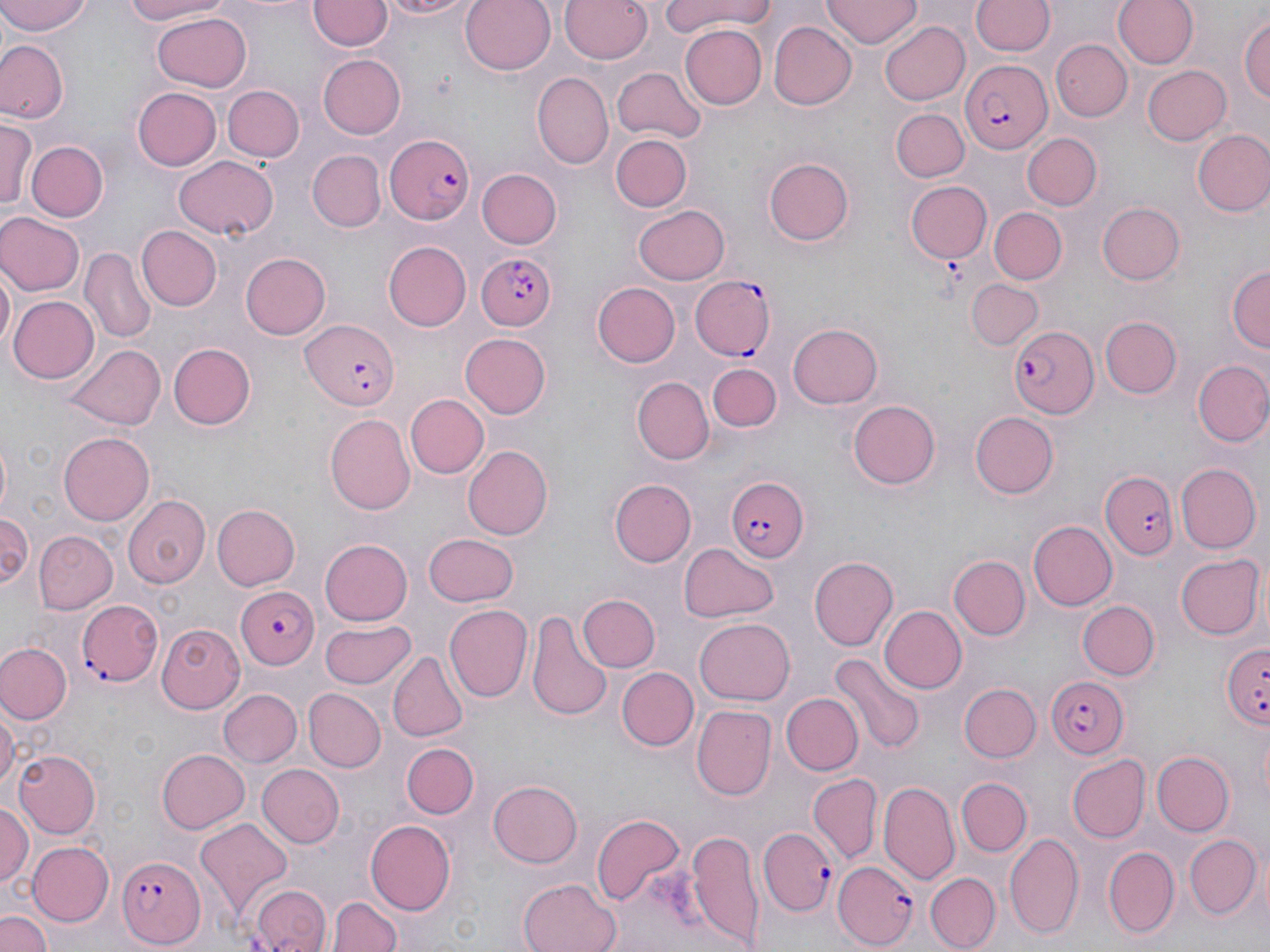

Approximate bounding boxes as (x1, y1, x2, y2) in pixels. Platelet locations: (937, 258, 969, 293). Plasmodium falciparum-infected red blood cell locations: (960, 59, 1052, 155), (382, 131, 473, 226), (473, 250, 558, 331), (690, 274, 776, 360), (301, 320, 399, 410), (1009, 324, 1100, 419), (1103, 472, 1175, 561), (725, 476, 808, 561), (234, 587, 320, 670), (76, 599, 162, 686), (1219, 642, 1268, 732), (1046, 676, 1130, 756), (757, 829, 834, 916), (118, 853, 205, 948), (832, 862, 920, 948). Uninfected red blood cell locations: (0, 0, 94, 36), (116, 0, 229, 25), (375, 0, 474, 18), (459, 0, 556, 75), (558, 0, 655, 63), (660, 0, 773, 37), (821, 0, 923, 49), (1114, 0, 1199, 70), (308, 1, 389, 52), (972, 1, 1054, 58), (152, 10, 251, 90), (1239, 10, 1270, 104), (881, 19, 970, 104), (769, 21, 857, 109), (678, 23, 767, 109), (0, 39, 68, 123), (1050, 39, 1131, 122), (317, 54, 407, 139), (1141, 66, 1232, 145), (613, 67, 706, 142), (535, 72, 615, 167), (221, 84, 304, 163), (133, 88, 221, 170), (891, 108, 968, 183), (0, 120, 34, 214), (1192, 128, 1270, 217), (1021, 133, 1101, 210), (610, 134, 692, 211), (26, 140, 109, 221), (308, 150, 386, 232), (173, 155, 278, 241), (765, 158, 855, 245), (475, 169, 559, 249), (906, 180, 993, 265), (1096, 201, 1184, 285), (634, 203, 731, 284), (989, 207, 1066, 285), (0, 212, 81, 296), (138, 225, 221, 310), (384, 242, 472, 330), (82, 246, 155, 345), (238, 251, 331, 340), (0, 264, 14, 358), (1227, 266, 1268, 355), (967, 279, 1044, 349), (594, 282, 680, 367), (9, 294, 99, 384), (1099, 316, 1180, 398), (788, 322, 883, 408), (459, 333, 552, 419), (168, 343, 257, 429), (65, 345, 165, 430), (1193, 360, 1270, 447), (707, 362, 781, 434), (633, 377, 712, 464), (406, 394, 488, 479), (847, 399, 942, 489), (969, 411, 1058, 498), (325, 413, 416, 516), (60, 432, 153, 525), (0, 433, 13, 518), (463, 445, 554, 539), (1174, 464, 1258, 552), (610, 479, 696, 566), (123, 493, 211, 589), (211, 503, 299, 590), (0, 512, 34, 592), (1027, 520, 1116, 611), (32, 531, 116, 614), (422, 532, 519, 606), (320, 539, 413, 626), (678, 542, 778, 623), (1174, 552, 1265, 641), (948, 556, 1030, 640), (808, 557, 897, 650), (579, 594, 660, 672), (1076, 599, 1160, 680), (444, 603, 531, 703), (880, 605, 967, 693), (527, 609, 613, 724), (695, 618, 796, 707), (321, 619, 416, 688), (154, 624, 243, 712), (1, 642, 72, 724), (389, 652, 468, 743), (833, 655, 923, 753), (616, 666, 699, 751), (960, 684, 1040, 762), (302, 687, 384, 773), (217, 688, 302, 768), (781, 694, 862, 774), (0, 701, 19, 800), (693, 707, 775, 801), (401, 741, 478, 820), (156, 748, 248, 833), (13, 750, 98, 839), (1152, 750, 1235, 834), (1067, 754, 1151, 842), (256, 765, 343, 848), (809, 773, 882, 863), (956, 777, 1031, 857), (487, 779, 582, 868), (879, 781, 960, 883), (0, 800, 32, 892), (591, 811, 687, 910), (195, 818, 294, 917), (365, 820, 456, 912), (685, 829, 768, 949), (1185, 833, 1261, 921), (1005, 834, 1083, 939), (26, 840, 114, 927), (1102, 845, 1180, 937), (926, 872, 999, 949), (518, 878, 624, 952), (248, 884, 331, 952), (332, 894, 402, 952), (0, 908, 50, 952). Slide-level diagnosis: Plasmodium falciparum. Light microscopy. May-Grünwald-Giemsa stain. Thin blood smear. 1000x magnification. One field of a larger specimen. Image is 1270×952 pixels.